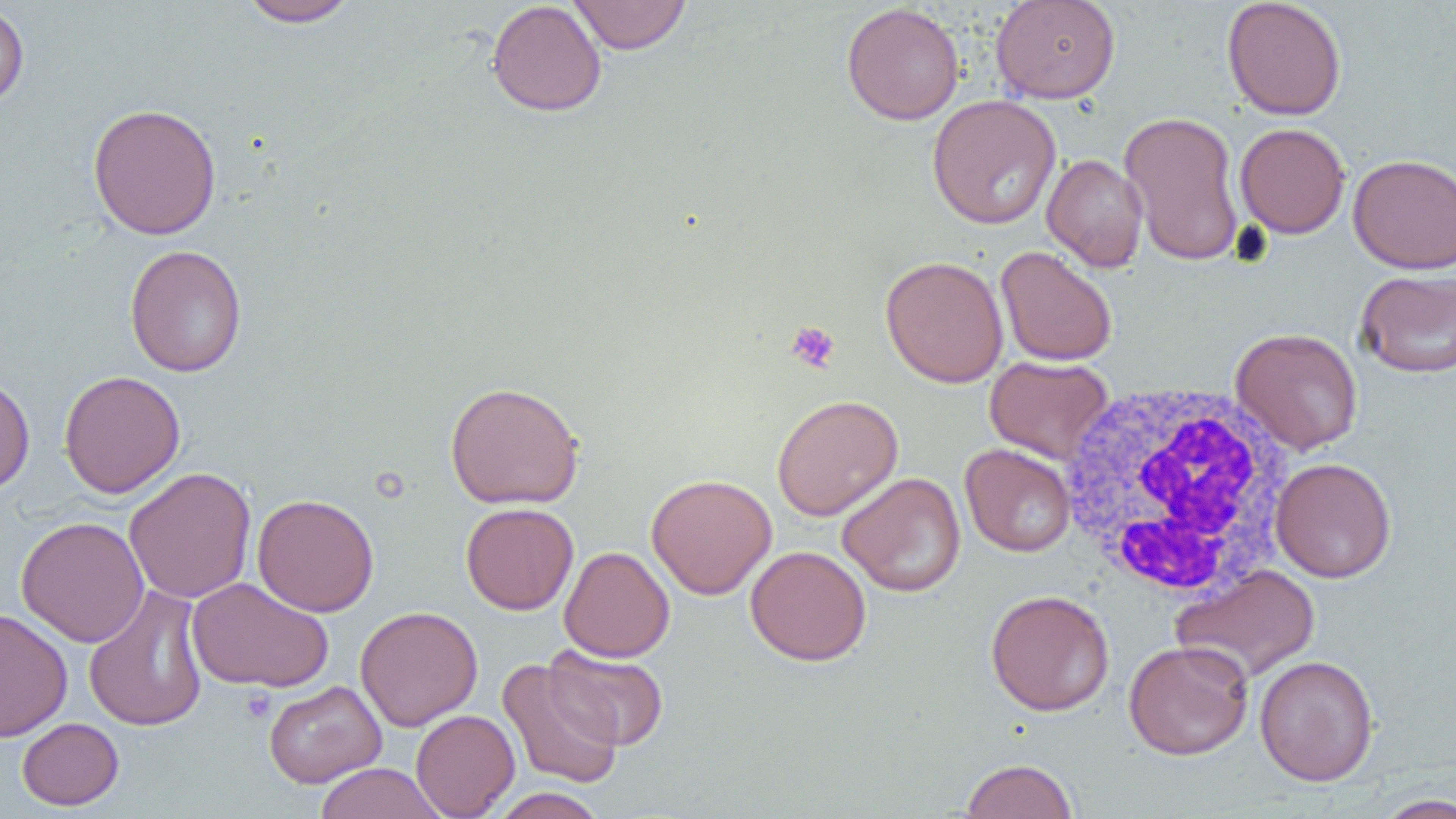
slide_level_diagnosis: negative for blood parasites
modality: optical microscopy
image_size: 1456×819 pixels
white_blood_cell_locations: 'approximate bounding boxes as (x1,y1)-(x2,y2) corner pairs in pixels: (1057,381)-(1299,600)'
uninfected_red_blood_cell_locations: 'approximate bounding boxes as (x1,y1)-(x2,y2) corner pairs in pixels: (237,0)-(360,27), (486,0)-(607,117), (567,0)-(691,54), (990,0)-(1120,104), (1221,0)-(1347,120), (0,3)-(29,111), (841,3)-(965,126), (926,94)-(1062,230), (87,102)-(222,240), (1119,110)-(1246,266), (1234,122)-(1350,239), (1347,153)-(1456,274), (1041,154)-(1148,272), (124,245)-(248,378), (995,246)-(1118,367), (880,255)-(1008,388), (1355,269)-(1456,378), (1230,327)-(1364,455), (985,355)-(1114,464), (58,369)-(186,498), (0,374)-(35,494), (445,380)-(584,509), (771,394)-(903,521), (960,443)-(1076,556), (1270,457)-(1397,582), (124,466)-(257,604), (837,472)-(966,597), (646,473)-(777,599), (252,493)-(379,616), (460,502)-(579,615), (15,516)-(149,647), (745,545)-(872,666), (559,546)-(674,662), (1171,564)-(1321,683), (186,577)-(334,693), (83,585)-(209,733), (985,589)-(1115,716), (355,605)-(483,731), (0,608)-(73,742), (1123,639)-(1254,760), (544,645)-(669,751), (1254,655)-(1379,786), (497,657)-(624,790), (263,679)-(386,788), (410,709)-(520,818), (17,717)-(124,810), (960,758)-(1078,819), (313,762)-(448,819), (490,787)-(606,819), (1373,793)-(1456,818)'
platelet_locations: 'approximate bounding boxes as (x1,y1)-(x2,y2) corner pairs in pixels: (785,321)-(840,373), (239,687)-(276,723)'
field_of_view: one of a larger specimen
preparation: thin blood film
magnification: 1000x